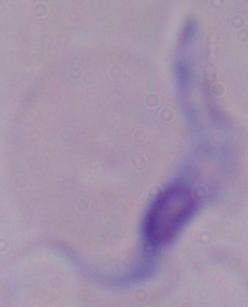
Photomicrograph. A trypanosome is shown. Captured at 1000x magnification.